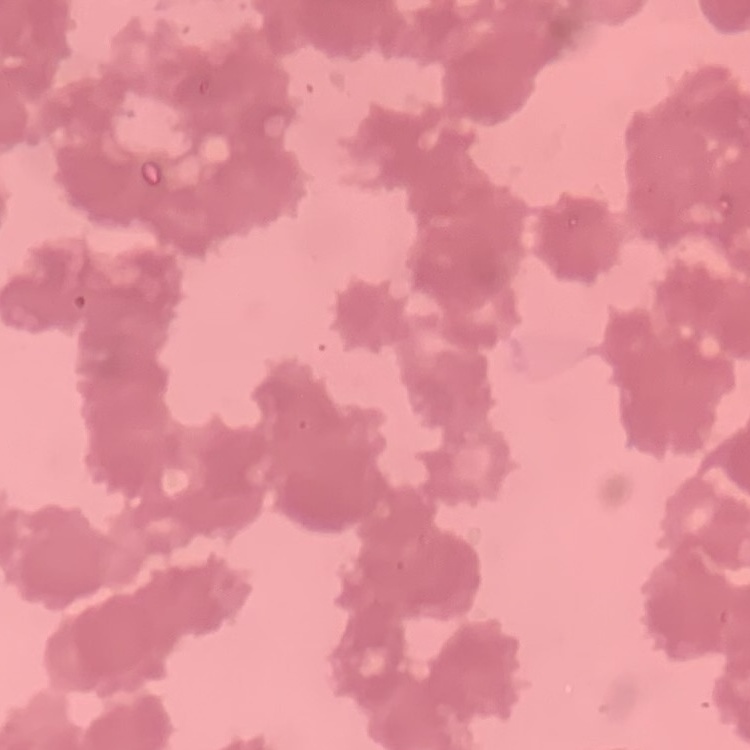
Summary:
  - Erythrocyte morphology: rouleaux formation
  - Stain: Field's or Giemsa
  - Image type: square crop of a larger photomicrograph
  - Preparation: thin peripheral smear